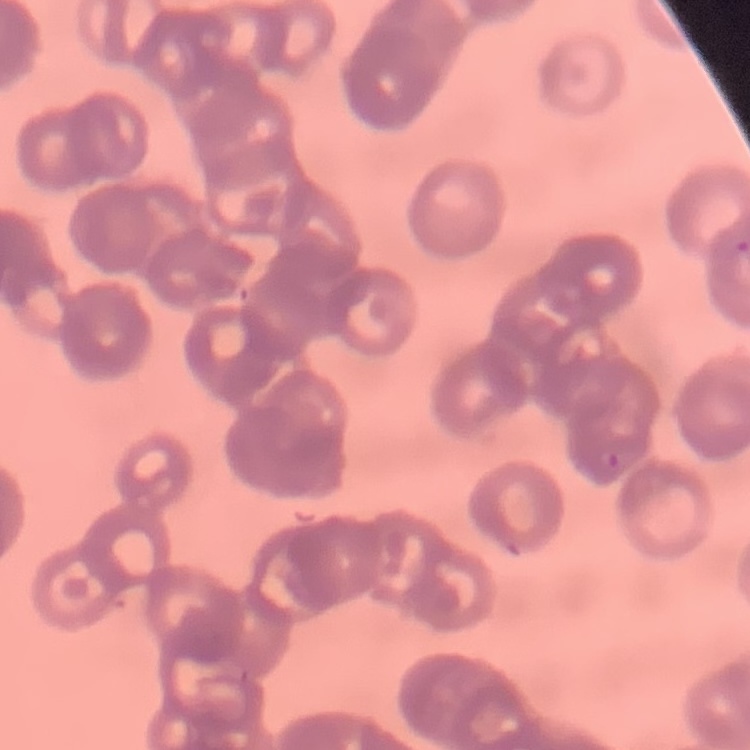
The erythrocytes exhibit rouleaux formation. Field's or Giemsa stain. Thin blood film. Square crop of a larger photomicrograph.